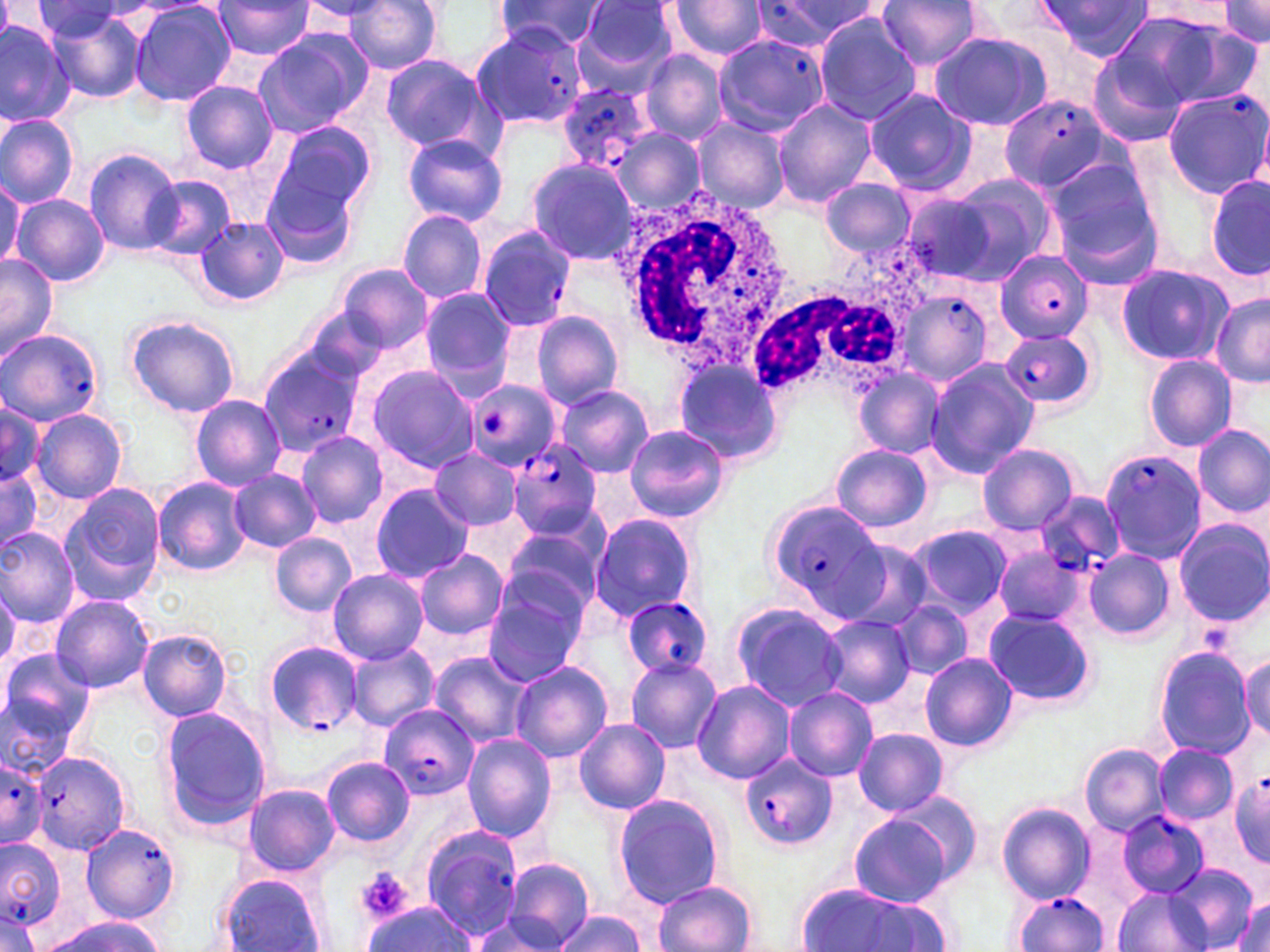
Approximate bounding boxes as [x1, y1, x2, y2] in pixels. Plasmodium falciparum-infected red blood cell locations: [755, 1, 881, 46], [471, 21, 592, 129], [712, 34, 829, 137], [557, 84, 655, 171], [996, 96, 1111, 192], [478, 226, 575, 330], [994, 249, 1093, 340], [898, 288, 993, 387], [1, 328, 103, 425], [999, 329, 1099, 410], [259, 349, 364, 457], [464, 379, 560, 471], [507, 444, 603, 540], [1099, 449, 1207, 563], [1037, 489, 1126, 577], [764, 501, 884, 618], [620, 595, 716, 679], [262, 640, 364, 737], [377, 702, 478, 799], [30, 751, 131, 855], [1, 754, 47, 847], [739, 754, 837, 850], [1228, 770, 1270, 865], [1117, 811, 1209, 898], [81, 823, 182, 923], [419, 824, 523, 939], [0, 836, 65, 931], [1011, 892, 1111, 951], [0, 908, 42, 952]. Platelet locations: [355, 869, 412, 922]. White blood cell locations: [617, 189, 786, 375], [750, 235, 936, 395]. Uninfected red blood cell locations: [212, 0, 314, 60], [874, 0, 988, 71], [1215, 0, 1270, 46], [298, 1, 394, 23], [343, 1, 446, 74], [495, 1, 610, 54], [572, 1, 681, 92], [666, 1, 768, 60], [1035, 1, 1156, 63], [127, 2, 236, 107], [1130, 3, 1246, 38], [27, 4, 134, 44], [41, 7, 149, 105], [1118, 10, 1256, 106], [812, 11, 921, 124], [0, 20, 77, 127], [250, 30, 370, 137], [927, 31, 1054, 132], [822, 33, 946, 180], [639, 51, 727, 144], [1086, 51, 1188, 149], [379, 54, 497, 155], [180, 80, 278, 173], [865, 89, 977, 195], [1162, 90, 1270, 199], [772, 97, 875, 207], [0, 111, 80, 209], [691, 118, 790, 214], [266, 120, 377, 223], [610, 128, 703, 216], [401, 132, 509, 225], [85, 147, 185, 255], [1040, 155, 1161, 275], [525, 157, 638, 263], [144, 173, 238, 260], [945, 175, 1058, 280], [1206, 176, 1270, 280], [264, 178, 358, 270], [819, 179, 915, 256], [0, 182, 22, 272], [900, 190, 1000, 286], [12, 194, 109, 287], [397, 210, 487, 301], [195, 216, 289, 308], [362, 223, 473, 328], [0, 255, 59, 361], [1116, 263, 1233, 365], [335, 264, 432, 352], [418, 288, 516, 389], [1211, 294, 1269, 387], [303, 308, 391, 385], [530, 311, 624, 408], [125, 315, 240, 418], [1144, 354, 1237, 452], [670, 360, 785, 466], [923, 360, 1039, 480], [366, 365, 479, 472], [853, 367, 945, 459], [554, 383, 654, 477], [190, 397, 287, 490], [1, 402, 45, 489], [31, 407, 128, 504], [624, 424, 729, 523], [1192, 424, 1270, 517], [295, 431, 389, 528], [977, 443, 1079, 534], [831, 444, 932, 531], [429, 448, 523, 532], [0, 464, 43, 555], [227, 469, 321, 552], [152, 477, 252, 576], [369, 484, 474, 581], [58, 485, 164, 607], [590, 512, 699, 621], [1174, 519, 1269, 626], [501, 525, 605, 616], [908, 525, 1014, 617], [0, 526, 80, 628], [270, 534, 356, 616], [834, 537, 934, 634], [990, 548, 1086, 628], [414, 549, 509, 640], [1084, 549, 1175, 641], [328, 569, 428, 664], [0, 576, 21, 671], [483, 589, 585, 687], [51, 595, 154, 692], [889, 599, 973, 681], [730, 603, 846, 711], [983, 609, 1094, 705], [819, 614, 914, 707], [138, 629, 233, 721], [346, 644, 440, 729], [1152, 646, 1257, 759], [428, 651, 531, 747], [0, 652, 91, 769], [920, 653, 1017, 752], [1239, 655, 1269, 740], [626, 658, 722, 752], [510, 661, 612, 762], [692, 681, 794, 784], [784, 687, 878, 782], [158, 704, 272, 837], [573, 718, 670, 815], [853, 727, 950, 815], [461, 734, 557, 841], [1080, 743, 1167, 833], [1153, 744, 1237, 824], [322, 757, 414, 846], [239, 782, 341, 879], [885, 789, 985, 886], [612, 794, 728, 909], [996, 801, 1095, 902], [847, 813, 954, 906], [502, 859, 594, 949], [1167, 863, 1259, 950], [218, 873, 326, 952], [652, 880, 757, 952], [1113, 884, 1210, 952], [798, 885, 947, 952], [1231, 891, 1270, 952], [362, 901, 479, 951], [552, 911, 646, 952], [467, 916, 563, 950], [40, 917, 170, 952]. Slide-level diagnosis: Plasmodium falciparum. Image is 1270×952 pixels. Captured at 1000x magnification. Single field of view. Thin blood smear. May-Grünwald-Giemsa stain. Light microscopy.